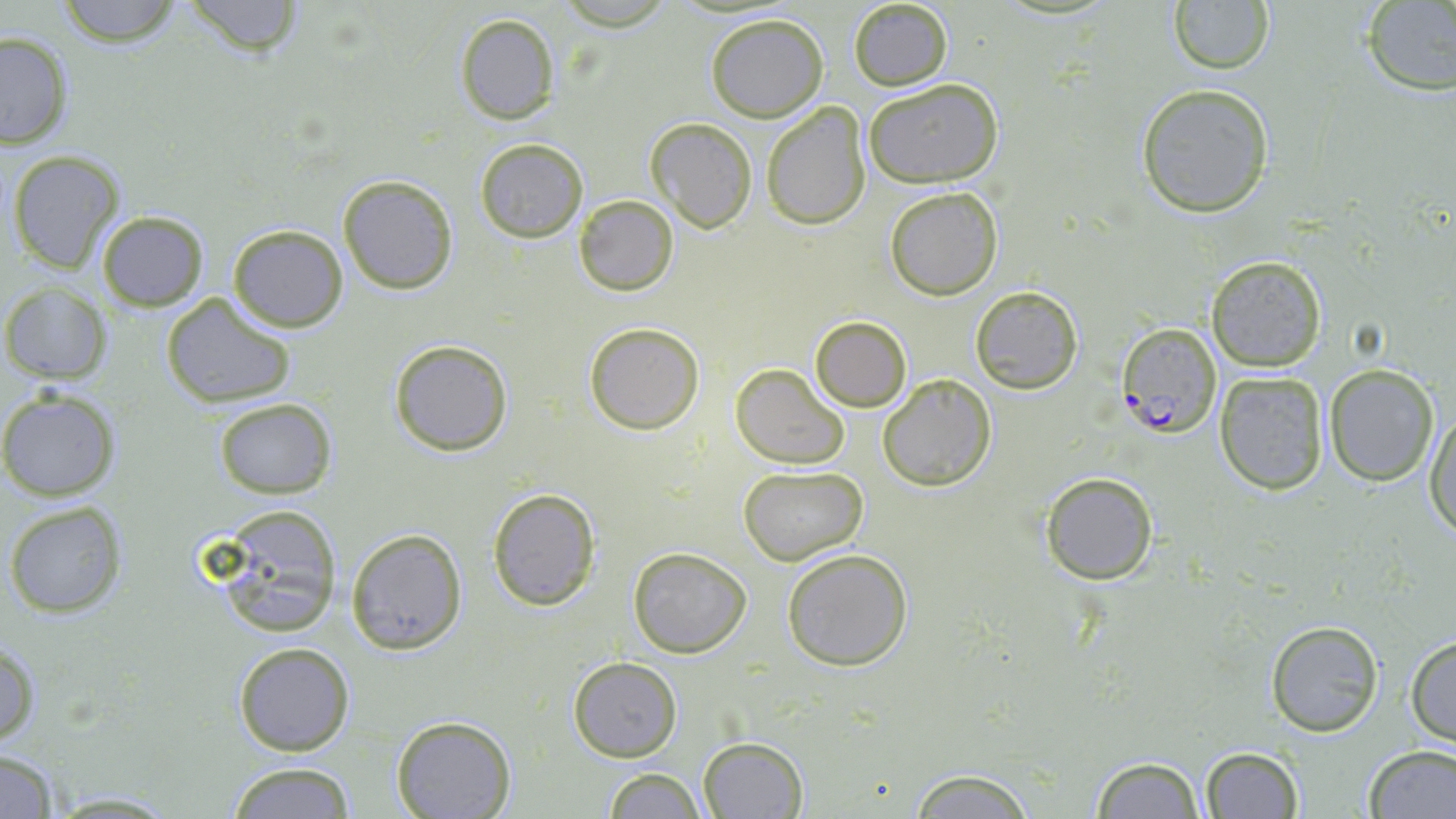 Approximate bounding boxes as (x1, y1, x2, y2) in pixels. Uninfected red blood cell locations: (183, 0, 304, 61), (1362, 0, 1456, 97), (54, 1, 185, 48), (846, 1, 955, 90), (1167, 2, 1276, 76), (454, 13, 560, 125), (705, 13, 828, 122), (0, 31, 75, 151), (863, 77, 1003, 189), (1135, 83, 1274, 217), (761, 102, 871, 230), (645, 118, 756, 234), (474, 139, 588, 242), (4, 150, 126, 275), (337, 174, 459, 294), (884, 186, 1003, 300), (573, 194, 678, 295), (96, 211, 209, 311), (227, 224, 348, 332), (1206, 256, 1326, 371), (2, 285, 112, 384), (969, 285, 1084, 393), (160, 294, 298, 407), (810, 316, 911, 411), (584, 321, 704, 435), (390, 339, 513, 457), (730, 364, 848, 469), (1324, 364, 1440, 486), (1214, 372, 1329, 496), (879, 374, 996, 491), (0, 390, 120, 501), (212, 398, 336, 498), (1426, 409, 1456, 539), (739, 466, 867, 565), (1040, 471, 1159, 586), (486, 489, 600, 611), (5, 501, 126, 619), (205, 507, 343, 639), (346, 527, 469, 655), (626, 546, 753, 658), (780, 548, 914, 670), (1265, 618, 1384, 738), (1405, 634, 1456, 746), (0, 640, 41, 750), (232, 641, 355, 756), (569, 656, 682, 763), (393, 715, 515, 819), (698, 737, 807, 818), (1363, 744, 1456, 818), (1200, 745, 1303, 818), (0, 750, 63, 818), (1088, 754, 1208, 819), (224, 763, 358, 818), (603, 766, 706, 819), (902, 766, 1043, 818), (43, 790, 188, 816). Plasmodium falciparum-infected red blood cell locations: (1119, 323, 1221, 439). Slide-level diagnosis: Plasmodium falciparum. Optical microscopy. Single field of view. Captured at 1000x magnification. Thin blood smear. Image is 1456×819 pixels. May-Grünwald-Giemsa-stained preparation.